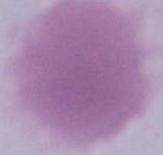 Photomicrograph. An erythrocyte is shown. 1000x magnification.